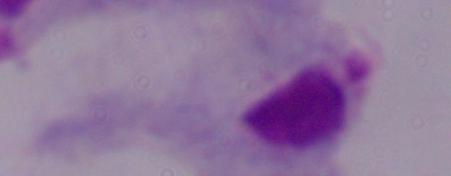
{
  "magnification": "1000x",
  "modality": "micrograph",
  "identification": "trichomonad"
}